Identify the cell.
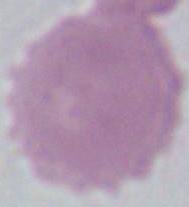

An erythrocyte.

magnification: 1000x
modality: micrograph